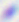

Summary:
  - Magnification: 400x
  - Identification: Toxoplasma gondii
  - Modality: micrograph